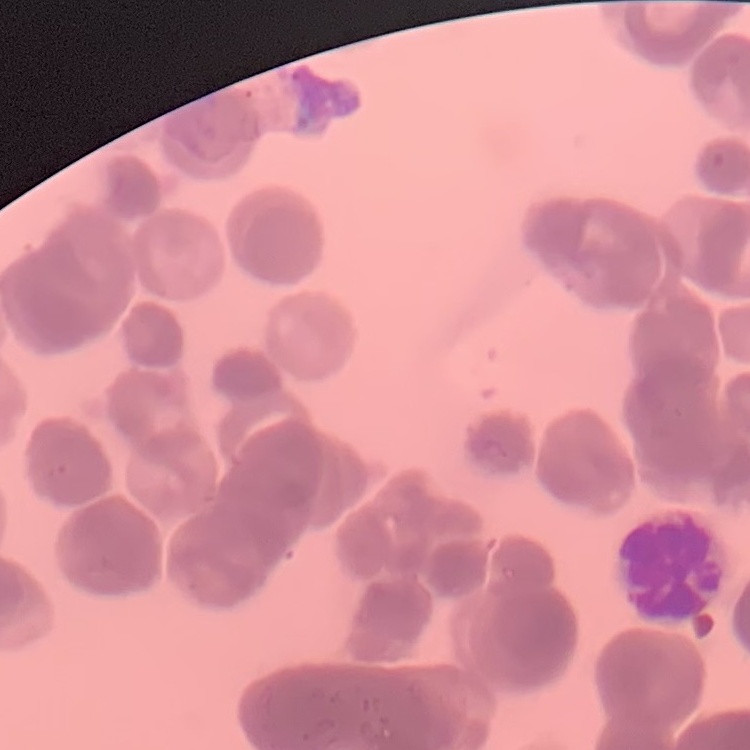
The red blood cells exhibit rouleaux formation. Square crop of a larger photomicrograph. Thin blood film. Stained with either Field's or Giemsa.